Give the extent of all Plasmodium ovale-infected red blood cells.
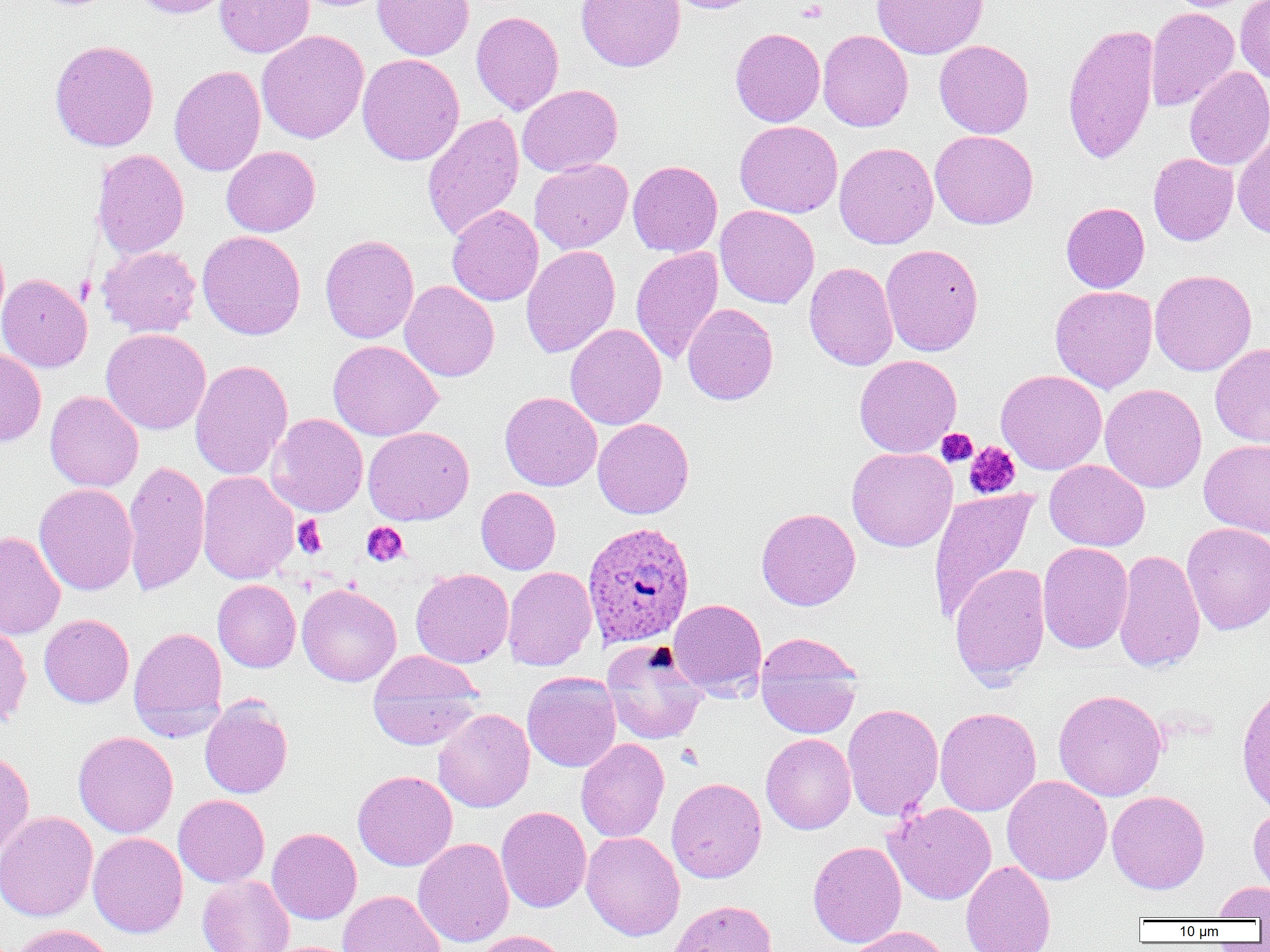

Approximate bounding boxes as [x1, y1, x2, y2] in pixels.
Plasmodium ovale-infected red blood cells: [582, 521, 696, 647].

{
  "slide_level_diagnosis": "Plasmodium ovale",
  "magnification": "1000x",
  "platelet_locations": "approximate bounding boxes as [x1, y1, x2, y2] in pixels: [797, 1, 828, 23], [936, 428, 977, 467], [964, 441, 1020, 499], [292, 515, 327, 559], [361, 522, 409, 567]",
  "modality": "optical microscopy",
  "uninfected_red_blood_cell_locations": "approximate bounding boxes as [x1, y1, x2, y2] in pixels: [132, 0, 233, 18], [215, 0, 315, 58], [372, 0, 474, 60], [576, 0, 685, 72], [665, 0, 764, 13], [871, 0, 989, 60], [1235, 0, 1270, 84], [1145, 6, 1239, 112], [471, 11, 564, 115], [1062, 23, 1159, 165], [730, 27, 825, 127], [256, 30, 369, 144], [817, 30, 913, 131], [49, 40, 159, 151], [933, 40, 1034, 138], [357, 53, 464, 166], [169, 65, 266, 176], [1184, 67, 1270, 170], [517, 84, 623, 177], [422, 113, 525, 242], [735, 121, 843, 218], [930, 129, 1038, 229], [1232, 131, 1270, 238], [834, 142, 938, 249], [221, 145, 320, 236], [92, 149, 189, 259], [1148, 153, 1238, 246], [529, 158, 632, 254], [628, 160, 723, 257], [1061, 202, 1150, 293], [447, 205, 544, 306], [714, 205, 819, 309], [197, 230, 306, 340], [320, 234, 420, 343], [880, 244, 984, 357], [98, 245, 201, 337], [521, 245, 620, 358], [631, 246, 724, 365], [804, 262, 898, 370], [1149, 269, 1257, 376], [0, 273, 92, 373], [399, 281, 499, 382], [1050, 285, 1157, 393], [682, 303, 778, 405], [565, 323, 667, 430], [101, 328, 211, 435], [328, 339, 443, 441], [1210, 343, 1270, 446], [0, 348, 46, 446], [854, 355, 962, 458], [190, 359, 293, 480], [996, 369, 1107, 475], [1099, 384, 1207, 493], [44, 390, 144, 492], [500, 392, 602, 491], [266, 413, 368, 517], [593, 418, 694, 519], [363, 426, 474, 526], [1199, 438, 1270, 538], [846, 447, 957, 552], [122, 460, 210, 596], [1044, 460, 1150, 551], [197, 471, 298, 584], [34, 483, 138, 595], [476, 486, 561, 574], [928, 488, 1037, 624], [756, 507, 861, 610], [1182, 522, 1270, 635], [0, 531, 66, 640], [1038, 542, 1133, 653], [1113, 549, 1206, 673], [949, 562, 1050, 686], [502, 566, 597, 671], [411, 568, 514, 668], [213, 580, 301, 672], [297, 584, 403, 686], [668, 598, 767, 699], [39, 614, 134, 708], [0, 623, 32, 729], [129, 627, 227, 736], [756, 637, 862, 739], [601, 639, 709, 745], [367, 651, 483, 749], [522, 671, 622, 772], [1237, 683, 1270, 817], [1054, 689, 1167, 801], [200, 698, 293, 799], [842, 703, 943, 821], [934, 707, 1042, 816], [433, 708, 534, 813], [73, 731, 178, 838], [761, 733, 856, 834], [576, 738, 669, 843], [0, 750, 34, 859], [353, 770, 457, 871], [1002, 775, 1112, 885], [666, 777, 767, 883], [1106, 790, 1210, 894], [173, 794, 270, 887], [884, 802, 997, 905], [1248, 803, 1270, 901], [496, 806, 591, 913], [0, 811, 98, 922], [267, 827, 361, 924], [581, 831, 685, 941], [88, 832, 188, 938], [413, 838, 515, 947], [807, 840, 906, 948], [960, 860, 1056, 952], [197, 875, 294, 952], [1211, 881, 1270, 920], [338, 890, 446, 952], [668, 900, 777, 951], [8, 924, 117, 952], [846, 926, 952, 952], [472, 930, 572, 952]",
  "image_size": "1270×952 pixels",
  "preparation": "thin blood smear",
  "field_of_view": "single"
}